Report the malaria status of this cell.
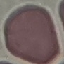
Uninfected.

capture = smartphone camera at the microscope eyepiece
preparation = thin smear
image type = cell patch, automatically extracted from a larger field of view and resized to 64 × 64 pixels
stain = Giemsa